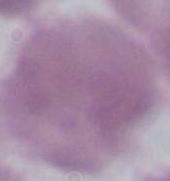

Summary:
  - Identification: erythrocyte
  - Modality: micrograph
  - Magnification: 1000x